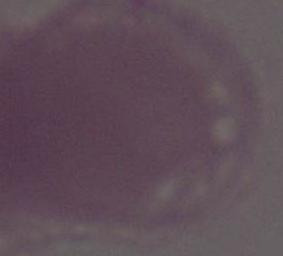 A red blood cell is shown. Photomicrograph. 1000x magnification.